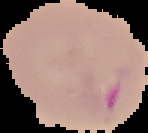
{
  "image_size": "148×133 pixels",
  "image_type": "cell region segmented out of the field of view; surrounding area masked to black",
  "preparation": "thin blood film",
  "malaria_status": "parasitized"
}